Assess this cell for malaria.
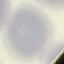

Uninfected.

Summary:
  - Stain: Giemsa
  - Image type: automatically extracted cell patch, resized to 64 × 64 pixels
  - Preparation: thin blood film
  - Capture: smartphone camera at the microscope eyepiece